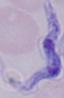
magnification = 1000x
identification = trypanosome
modality = micrograph